Report the malaria status of this cell.
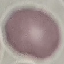

It is uninfected.

Automatically extracted cell patch, resized to 64 × 64 pixels. Giemsa stain. Thin smear of blood. Acquired by smartphone through the microscope eyepiece.